Give the position of every malaria parasite.
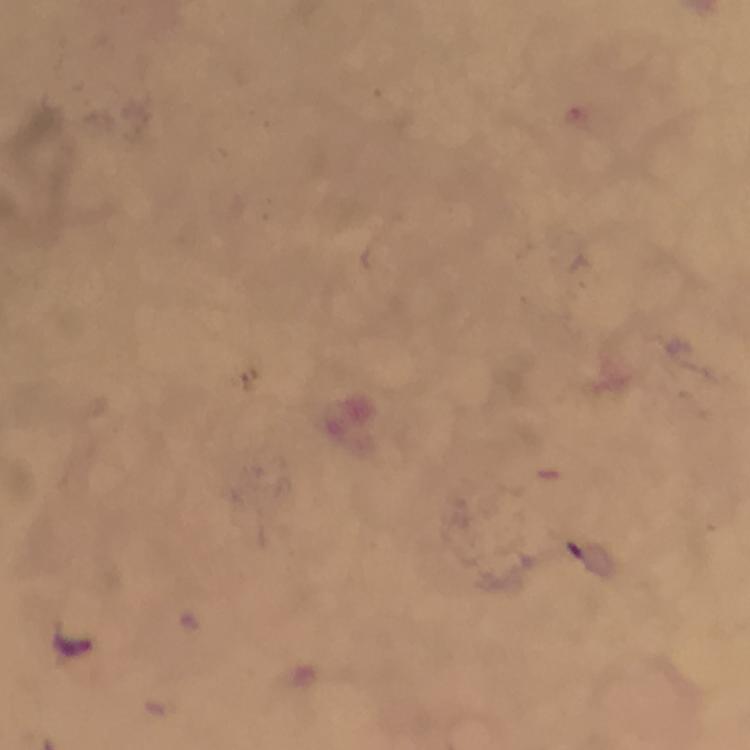
Approximate centers as {x, y} in pixels.
Malaria parasites: {74, 646}.

Giemsa stain. At 100x magnification. Immersion oil was used. From a malaria diagnostic workup. Smartphone photograph taken through a microscope. Image is 750×750 pixels. A crop from one field of view. Thick blood smear.